Identify the blood parasite species.
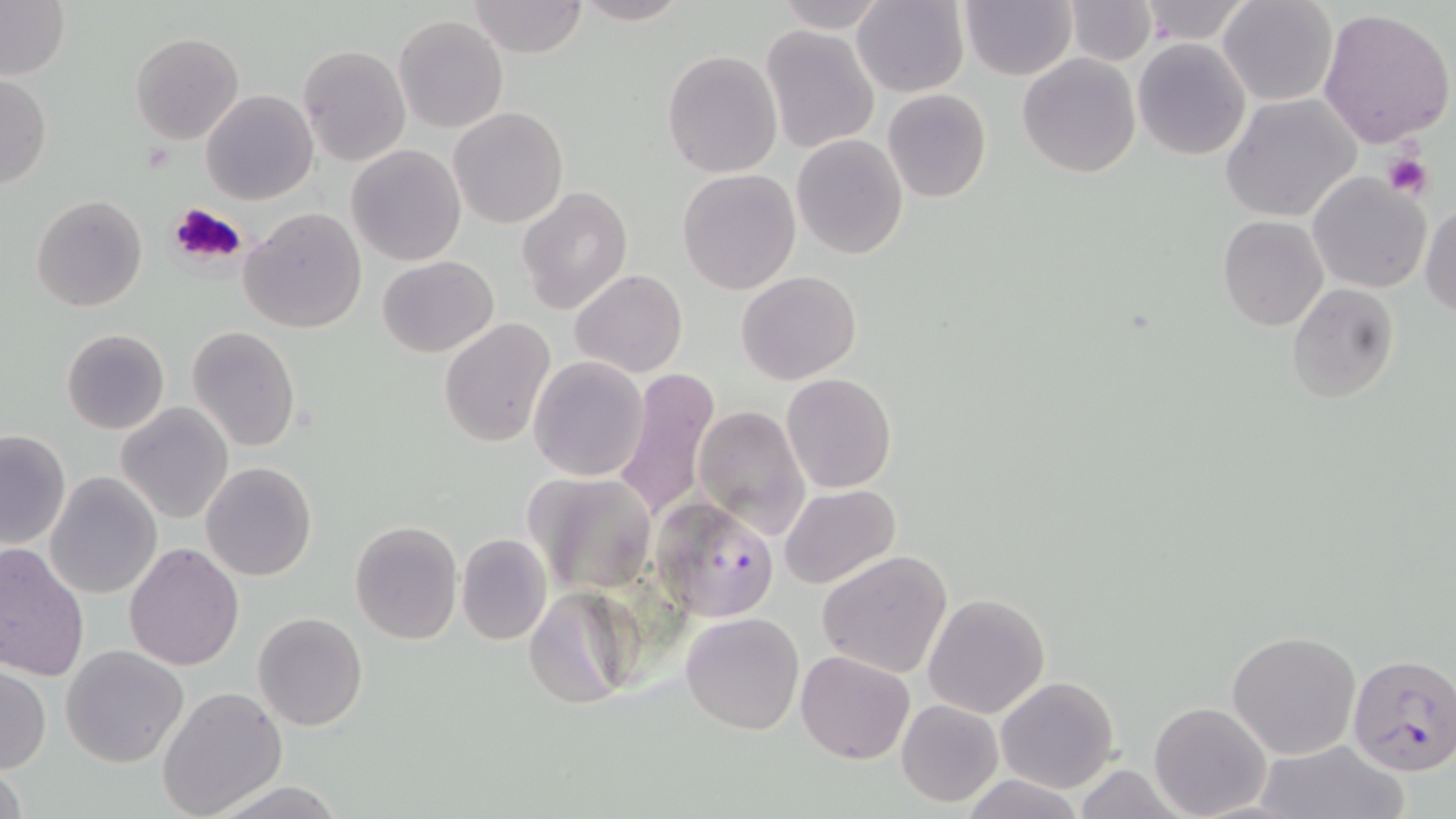

Plasmodium falciparum.

image size = 1456×819 pixels
magnification = 1000x
modality = light microscopy
uninfected red blood cell locations = approximate bounding boxes as (x1, y1, x2, y2) in pixels: (467, 0, 588, 57), (569, 0, 692, 26), (772, 0, 890, 31), (852, 0, 969, 98), (958, 0, 1077, 81), (1065, 0, 1157, 65), (1220, 0, 1338, 106), (0, 1, 70, 80), (1135, 1, 1253, 45), (1318, 6, 1455, 147), (394, 15, 508, 133), (761, 24, 882, 154), (130, 31, 244, 145), (1133, 37, 1251, 159), (297, 43, 410, 167), (662, 49, 782, 178), (1017, 53, 1142, 178), (0, 74, 51, 190), (881, 88, 992, 203), (201, 90, 317, 207), (1221, 94, 1360, 223), (448, 107, 568, 229), (791, 133, 908, 259), (348, 145, 466, 265), (677, 169, 801, 295), (1308, 173, 1430, 294), (517, 188, 633, 314), (30, 194, 148, 312), (1420, 203, 1455, 316), (238, 207, 367, 334), (1218, 215, 1329, 332), (378, 255, 500, 357), (570, 269, 688, 378), (736, 272, 862, 386), (1286, 282, 1399, 403), (438, 317, 557, 448), (188, 325, 302, 451), (60, 329, 170, 434), (529, 357, 649, 480), (616, 366, 720, 521), (782, 372, 897, 493), (117, 402, 234, 523), (694, 404, 811, 538), (0, 429, 71, 550), (201, 462, 316, 582), (524, 470, 662, 595), (45, 472, 162, 597), (778, 484, 901, 589), (350, 520, 462, 644), (456, 532, 551, 645), (0, 541, 90, 683), (123, 542, 245, 670), (816, 550, 954, 679), (523, 586, 642, 711), (923, 593, 1050, 719), (253, 611, 369, 730), (680, 611, 804, 735), (1227, 630, 1361, 758), (61, 645, 187, 766), (796, 649, 916, 764), (0, 665, 51, 774), (995, 675, 1121, 793), (157, 685, 288, 819), (897, 699, 1003, 806), (1148, 701, 1273, 819), (1252, 739, 1407, 819), (0, 756, 30, 819), (963, 774, 1085, 819), (207, 779, 349, 818)
Plasmodium falciparum-infected red blood cell locations = approximate bounding boxes as (x1, y1, x2, y2) in pixels: (652, 496, 779, 621), (1346, 652, 1456, 775)
field of view = single
stain = May-Grünwald-Giemsa
platelet locations = approximate bounding boxes as (x1, y1, x2, y2) in pixels: (1382, 154, 1430, 200), (167, 201, 250, 269)
preparation = thin blood film